Identify the blood parasite species.
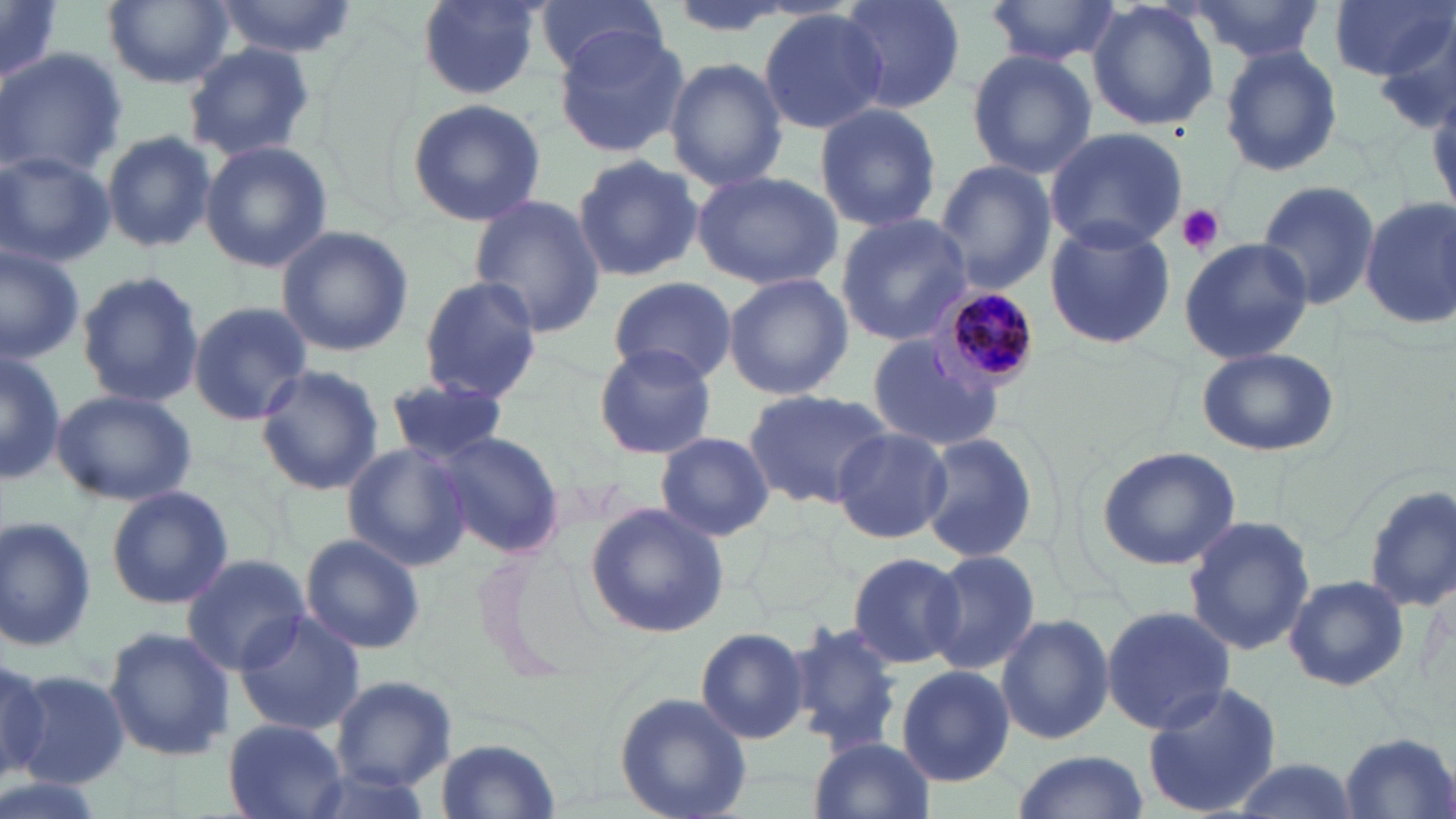

Plasmodium malariae.

Approximate bounding boxes as (x1, y1, x2, y2) in pixels. Uninfected red blood cell locations: (1, 0, 62, 89), (210, 0, 363, 61), (411, 0, 545, 100), (528, 0, 670, 78), (837, 0, 966, 113), (982, 0, 1122, 70), (1087, 0, 1221, 133), (1188, 0, 1326, 66), (1330, 0, 1451, 79), (104, 1, 232, 89), (758, 8, 887, 136), (1370, 18, 1456, 129), (552, 25, 690, 159), (183, 44, 316, 160), (1218, 46, 1345, 177), (0, 49, 125, 179), (966, 50, 1097, 178), (664, 57, 789, 191), (406, 98, 547, 227), (813, 102, 943, 234), (1045, 126, 1186, 253), (102, 131, 217, 253), (200, 140, 333, 274), (0, 149, 116, 269), (572, 153, 703, 283), (934, 160, 1056, 293), (691, 169, 844, 290), (1255, 178, 1381, 311), (468, 195, 605, 336), (1360, 197, 1456, 329), (834, 212, 973, 348), (1045, 219, 1175, 350), (276, 226, 414, 358), (1177, 235, 1316, 366), (0, 243, 84, 362), (75, 268, 205, 410), (722, 272, 853, 400), (417, 274, 543, 402), (608, 276, 736, 384), (186, 301, 312, 427), (867, 335, 1005, 453), (592, 342, 717, 460), (1193, 345, 1339, 456), (0, 348, 63, 486), (256, 365, 384, 495), (386, 374, 509, 465), (742, 387, 899, 508), (50, 388, 197, 505), (831, 427, 952, 543), (433, 430, 563, 557), (916, 431, 1040, 563), (656, 432, 775, 540), (343, 443, 472, 572), (1098, 444, 1243, 571), (105, 484, 233, 609), (1364, 485, 1455, 612), (584, 501, 730, 638), (0, 515, 100, 651), (1183, 516, 1318, 655), (299, 533, 430, 654), (924, 549, 1042, 679), (847, 551, 966, 669), (181, 553, 310, 673), (1282, 574, 1412, 692), (1101, 605, 1237, 733), (232, 610, 367, 735), (996, 612, 1115, 746), (695, 624, 808, 746), (785, 624, 903, 755), (103, 626, 235, 762), (0, 659, 54, 778), (896, 665, 1015, 787), (15, 671, 130, 790), (330, 674, 457, 792), (1141, 681, 1284, 818), (613, 691, 749, 819), (224, 718, 347, 817), (1338, 732, 1455, 818), (435, 735, 561, 817), (807, 736, 937, 819), (1011, 750, 1150, 819), (1224, 756, 1361, 818). Platelet locations: (1177, 205, 1226, 256). Plasmodium malariae-infected red blood cell locations: (935, 287, 1044, 396). May-Grünwald-Giemsa stain. Image is 1456×819 pixels. One field of a larger specimen. Light microscopy. Thin blood smear. Captured at 1000x magnification.